Draw a bounding box around every leukocyte (white blood cell).
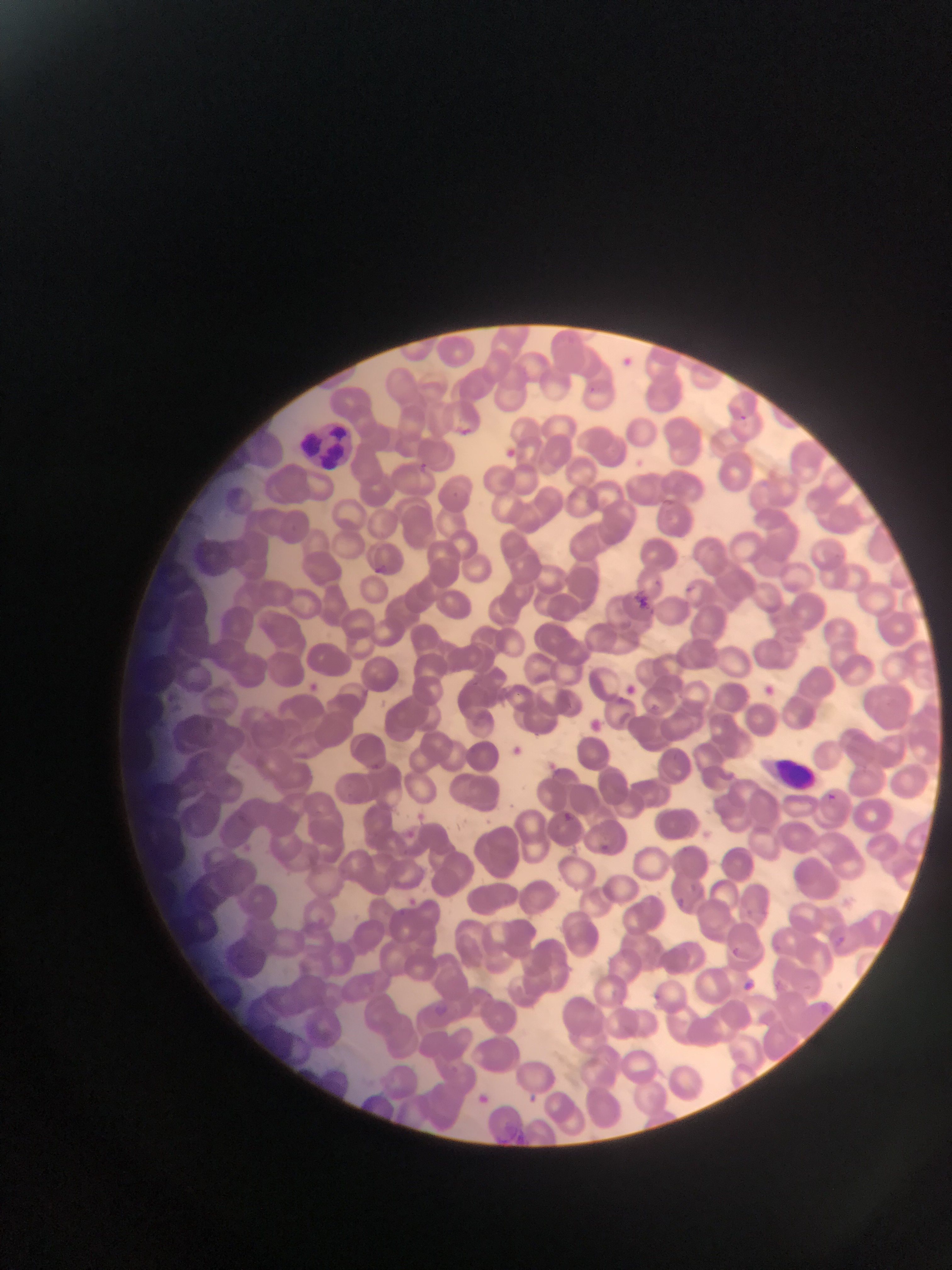
Approximate bounding boxes as {left, top, right, bottom} in pixels.
Leukocytes: {303, 419, 355, 466}, {759, 740, 816, 791}.

capture: mobile-phone photograph through a microscope
image_size: 952×1270 pixels
country: Ghana
preparation: thin blood smear
malaria_parasite_locations: 'approximate bounding boxes as {left, top, right, bottom} in pixels: {621, 355, 635, 372}, {738, 412, 747, 425}, {460, 426, 474, 440}, {506, 446, 517, 459}, {636, 457, 644, 469}, {417, 460, 431, 475}, {373, 562, 385, 574}, {651, 575, 657, 585}, {684, 582, 701, 596}, {631, 593, 656, 607}, {622, 681, 639, 702}, {764, 682, 776, 701}, {588, 718, 609, 743}, {510, 741, 527, 759}, {547, 758, 568, 774}, {823, 791, 835, 808}, {564, 803, 578, 817}, {411, 809, 425, 821}, {403, 828, 418, 841}, {596, 839, 608, 851}, {690, 881, 698, 893}, {404, 895, 425, 909}, {677, 895, 682, 909}, {833, 933, 844, 947}, {727, 943, 742, 958}, {740, 976, 752, 990}, {529, 1089, 546, 1102}, {470, 1093, 487, 1104}, {505, 1119, 522, 1133}'
field_of_view: single